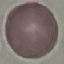 Malaria status: uninfected. Giemsa stain. Thin blood film. Automatically extracted cell patch, resized to 64 × 64 pixels. Acquired by smartphone through the microscope eyepiece.